Describe the morphology of the erythrocytes.
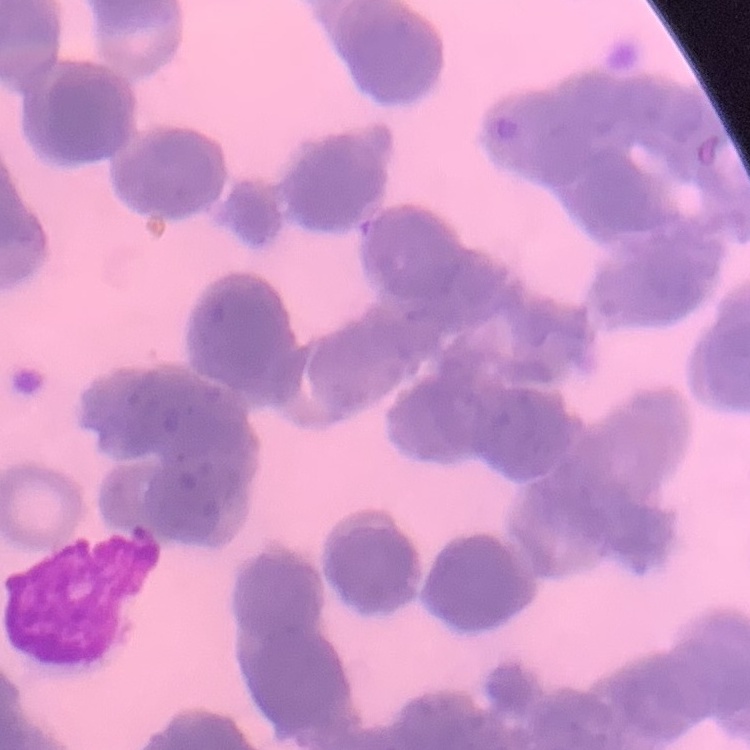
They show rouleaux formation.

Summary:
  - Stain: Field's or Giemsa
  - Image type: square crop of a larger photomicrograph
  - Preparation: thin peripheral smear